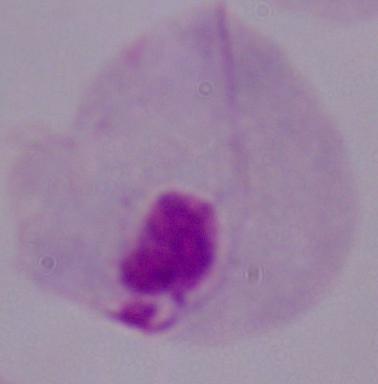

identification = trichomonad
modality = micrograph
magnification = 1000x